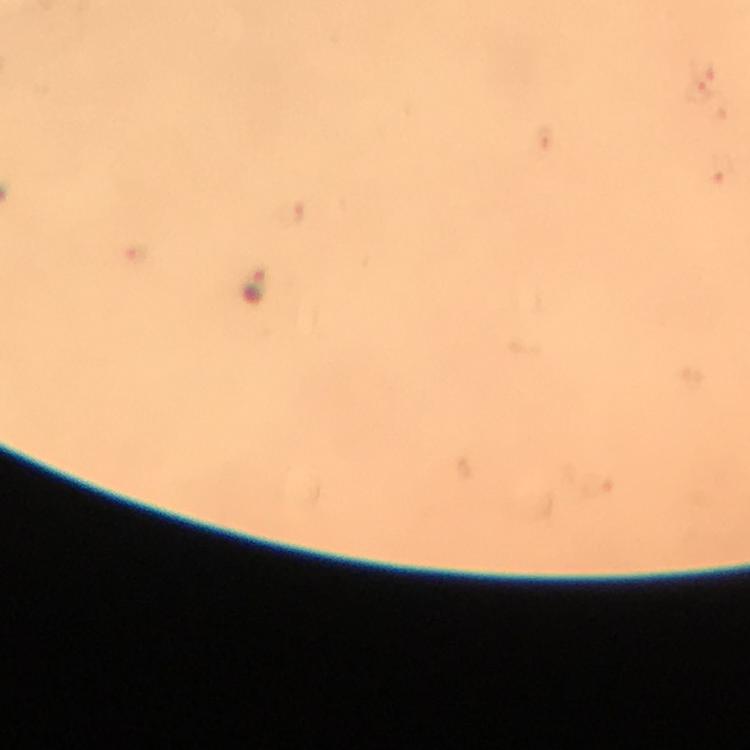
Approximate centers as (x, y) in pixels. Plasmodium parasite locations: (699, 92), (255, 286). Image is 750×750 pixels. Immersion oil applied. From a diagnostic examination for malaria. 100x magnification. Thick blood smear. Giemsa stain. Cropped region of a single field of view. Photographed with a smartphone mounted on the microscope.